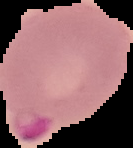 From a thin blood film. Result: Plasmodium parasites detected. Cell region segmented out of the field of view; the surrounding area is masked to black. Image is 133×148 pixels.